Identify the blood parasite species.
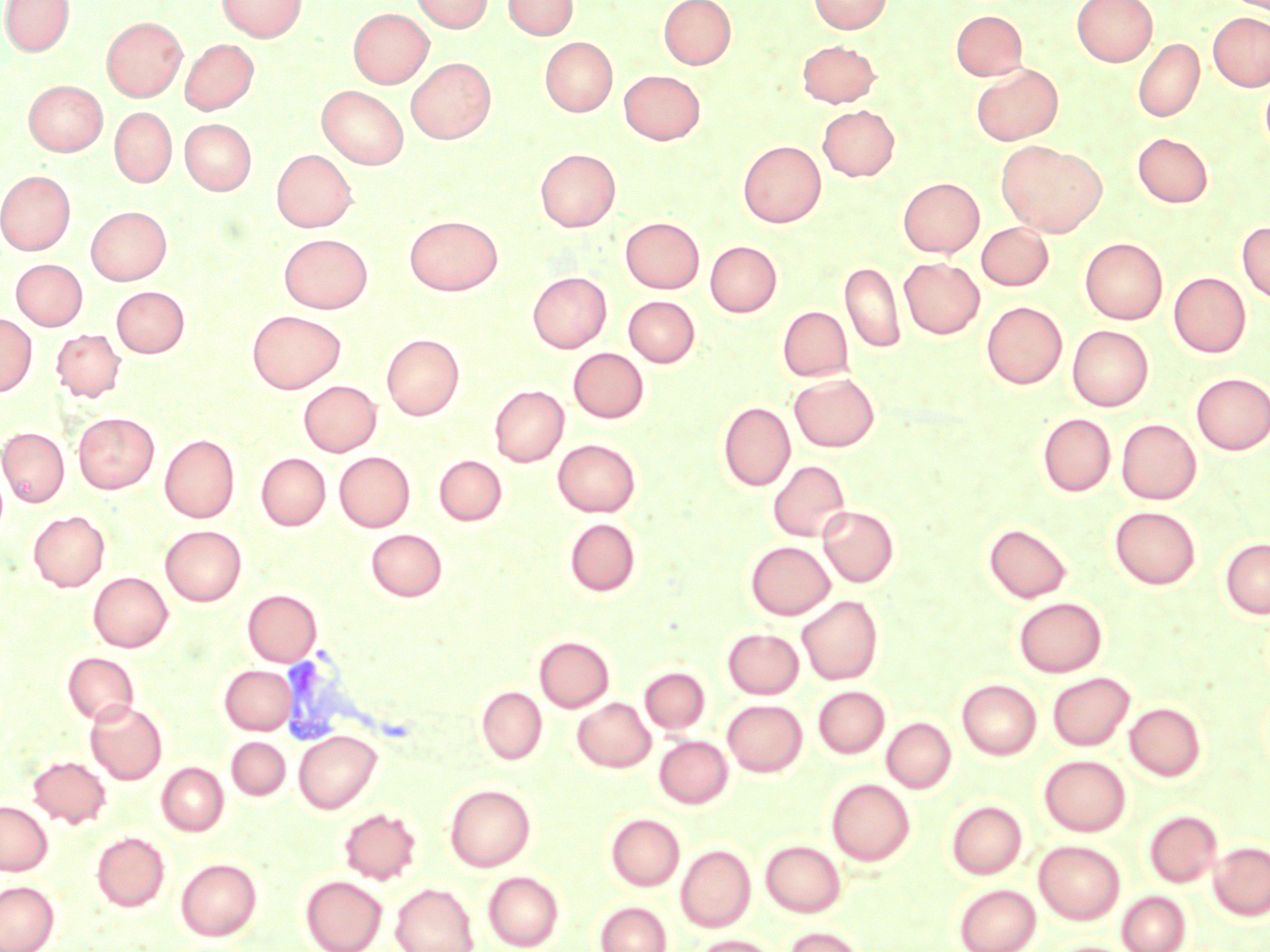
Plasmodium vivax.

Summary:
  - Coordinate format: approximate bounding boxes as (x1,y1)-(x2,y2) corner pairs in pixels
  - Plasmodium vivax-infected red blood cell locations: (281,647)-(381,737)
  - Uninfected red blood cell locations: (1,0)-(74,56), (217,0)-(307,41), (411,0)-(492,33), (503,0)-(577,39), (658,0)-(736,69), (809,0)-(891,34), (1072,0)-(1156,66), (349,8)-(433,87), (951,10)-(1027,80), (1209,12)-(1270,91), (102,17)-(186,101), (540,37)-(616,116), (1133,38)-(1204,122), (180,39)-(258,115), (797,40)-(880,107), (406,57)-(496,143), (971,63)-(1063,145), (619,70)-(704,144), (1261,73)-(1270,160), (24,81)-(108,155), (317,85)-(409,169), (818,105)-(899,181), (110,107)-(176,188), (180,118)-(256,194), (1133,133)-(1212,207), (738,141)-(826,227), (997,141)-(1106,237), (272,149)-(357,232), (535,149)-(620,231), (0,170)-(75,255), (899,178)-(984,257), (86,206)-(172,285), (405,215)-(502,295), (621,217)-(704,293), (1237,221)-(1270,304), (977,222)-(1053,290), (279,233)-(373,313), (1080,237)-(1167,324), (705,241)-(781,317), (899,258)-(984,338), (12,259)-(87,330), (841,261)-(906,353), (528,272)-(611,353), (1169,272)-(1250,357), (111,286)-(189,357), (623,296)-(700,367), (982,301)-(1066,388), (778,306)-(853,381), (247,310)-(345,393), (0,313)-(36,396), (1067,326)-(1153,410), (51,328)-(126,402), (382,333)-(464,420), (568,348)-(648,423), (790,373)-(879,452), (1191,373)-(1270,454), (298,380)-(382,456), (489,385)-(569,466), (719,401)-(795,491), (73,412)-(159,492), (1038,413)-(1115,496), (1117,419)-(1201,504), (0,427)-(69,506), (160,434)-(239,522), (553,438)-(640,517), (335,452)-(414,531), (257,453)-(330,529), (434,455)-(507,525), (768,460)-(851,541), (818,505)-(899,587), (1109,506)-(1201,589), (28,510)-(110,591), (565,517)-(640,596), (984,522)-(1072,603), (161,525)-(246,605), (366,528)-(447,601), (1220,538)-(1270,618), (746,541)-(834,619), (88,572)-(172,651), (243,590)-(321,666), (797,595)-(883,685), (1014,597)-(1107,677), (723,628)-(804,698), (535,636)-(614,712), (62,652)-(140,725), (220,665)-(295,734), (640,667)-(710,733), (1048,672)-(1135,750), (957,679)-(1041,759), (477,686)-(547,764), (814,686)-(889,758), (573,698)-(655,771), (85,700)-(167,784), (724,700)-(807,776), (1125,702)-(1206,781), (882,718)-(956,793), (293,730)-(381,813), (654,736)-(732,808), (227,737)-(290,800), (28,755)-(111,828), (1040,755)-(1130,836), (157,762)-(229,835), (827,779)-(915,865), (444,784)-(535,871), (947,800)-(1027,879), (0,801)-(52,875), (339,807)-(421,884), (1144,810)-(1222,887), (606,814)-(684,890), (91,832)-(169,911), (761,840)-(846,917), (1034,841)-(1125,924), (1209,841)-(1270,920), (676,845)-(756,932), (176,858)-(262,940), (483,871)-(564,951), (301,876)-(387,951), (0,880)-(59,952), (390,883)-(479,952), (953,883)-(1042,952), (1117,891)-(1191,952), (596,901)-(671,952), (783,926)-(866,952), (694,935)-(777,952)
  - Stain: May-Grünwald-Giemsa
  - Magnification: 1000x
  - Preparation: thin blood smear
  - Image size: 1270×952 pixels
  - Field of view: single
  - Modality: optical microscopy